Evaluate for malaria.
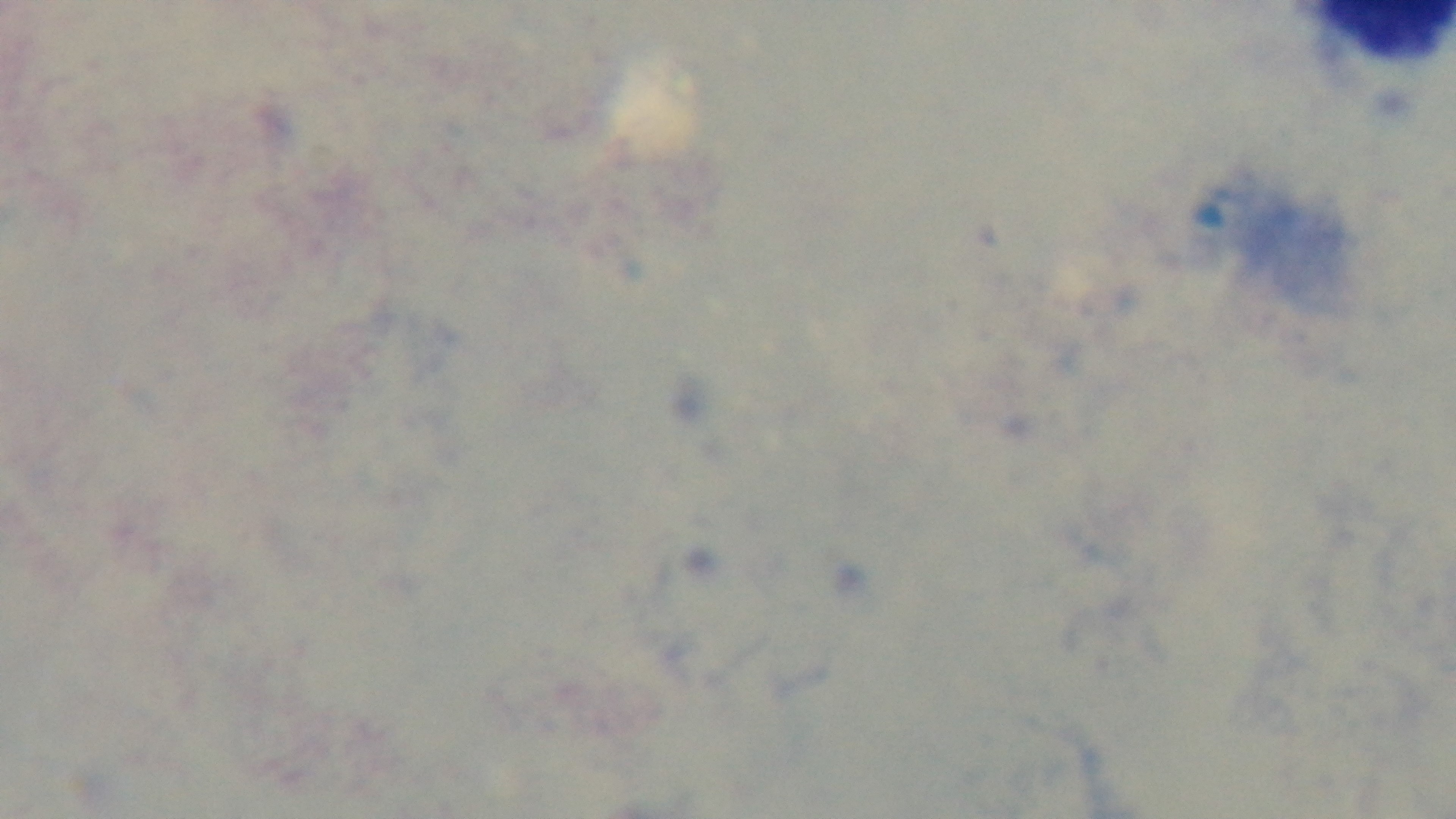
Negative.

preparation = thick blood film
stain = Giemsa
field of view = single
objective = 100x oil immersion
capture = mounted 4K digital camera
modality = light microscopy